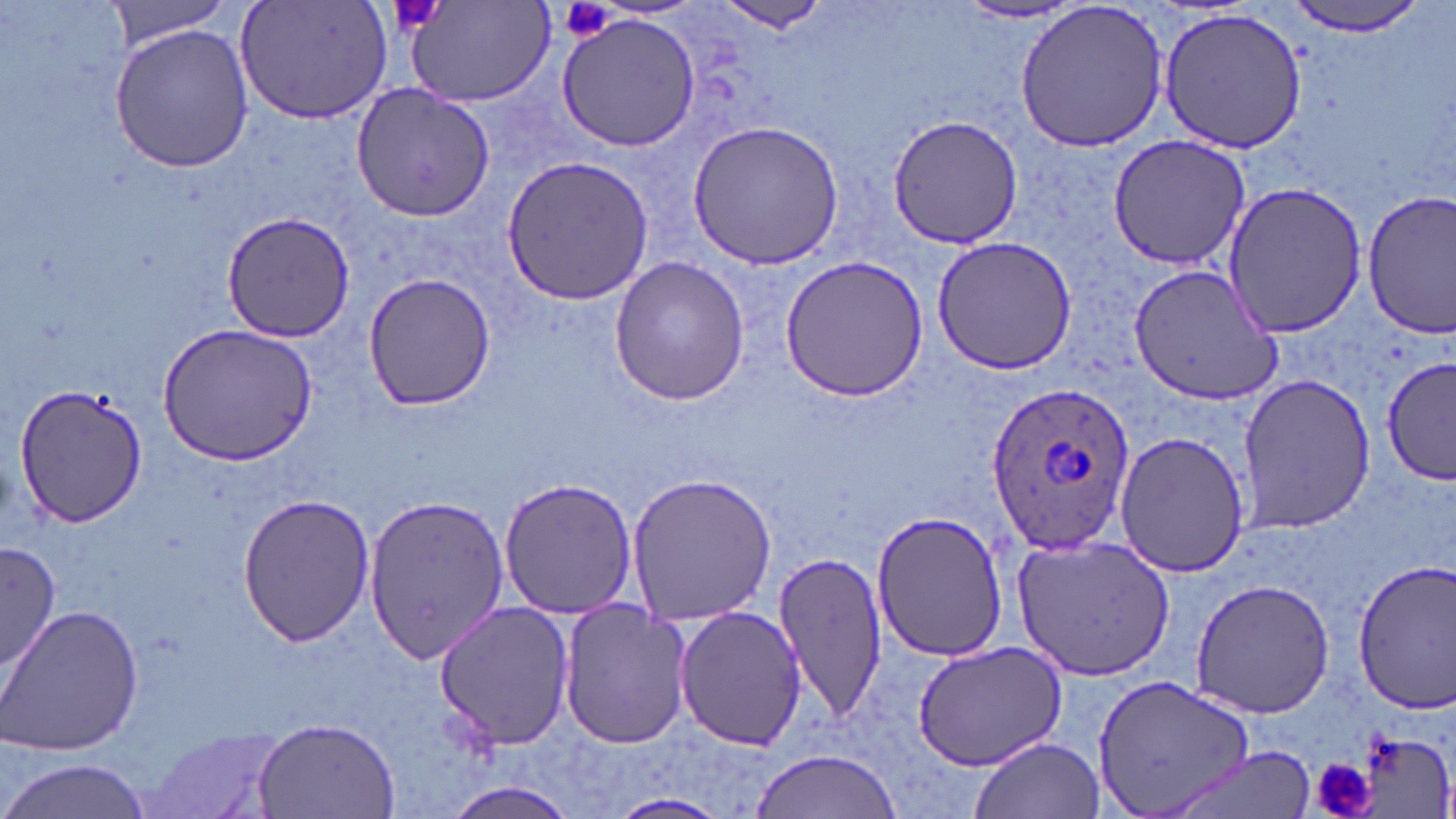 Approximate bounding boxes as [x1, y1, x2, y2] in pixels. Plasmodium ovale-infected red blood cell locations: [986, 383, 1135, 554]. Uninfected red blood cell locations: [402, 0, 556, 108], [1013, 0, 1172, 153], [1280, 0, 1432, 36], [104, 1, 234, 48], [234, 1, 394, 124], [706, 2, 836, 36], [955, 3, 1086, 25], [1155, 5, 1310, 155], [556, 13, 702, 153], [109, 21, 255, 173], [352, 84, 492, 221], [890, 115, 1021, 249], [685, 120, 846, 271], [1106, 136, 1250, 267], [497, 156, 654, 308], [1221, 181, 1367, 339], [1361, 190, 1455, 340], [221, 212, 354, 340], [931, 236, 1076, 376], [608, 254, 753, 406], [779, 255, 929, 401], [1128, 263, 1284, 407], [362, 272, 495, 412], [160, 323, 319, 463], [1379, 356, 1455, 486], [1235, 372, 1376, 535], [11, 382, 148, 530], [1114, 430, 1249, 578], [624, 470, 776, 627], [498, 477, 639, 619], [364, 490, 511, 668], [236, 492, 374, 647], [870, 509, 1008, 663], [1010, 533, 1174, 681], [2, 539, 58, 679], [774, 548, 887, 726], [1354, 556, 1456, 718], [1191, 578, 1332, 719], [432, 599, 575, 751], [558, 599, 695, 749], [0, 603, 145, 758], [672, 605, 807, 751], [913, 641, 1068, 771], [1093, 673, 1252, 816], [251, 718, 402, 818], [145, 727, 286, 819], [1347, 729, 1451, 819], [970, 735, 1103, 819], [1165, 749, 1321, 816], [748, 750, 906, 819], [1, 757, 156, 819], [436, 782, 584, 818], [607, 792, 734, 819]. Platelet locations: [388, 0, 447, 33], [560, 0, 614, 41], [1312, 757, 1372, 819]. Slide-level diagnosis: Plasmodium ovale. Image is 1456×819 pixels. Single field of view. May-Grünwald-Giemsa stain. 1000x magnification. Thin blood smear. Optical microscopy.